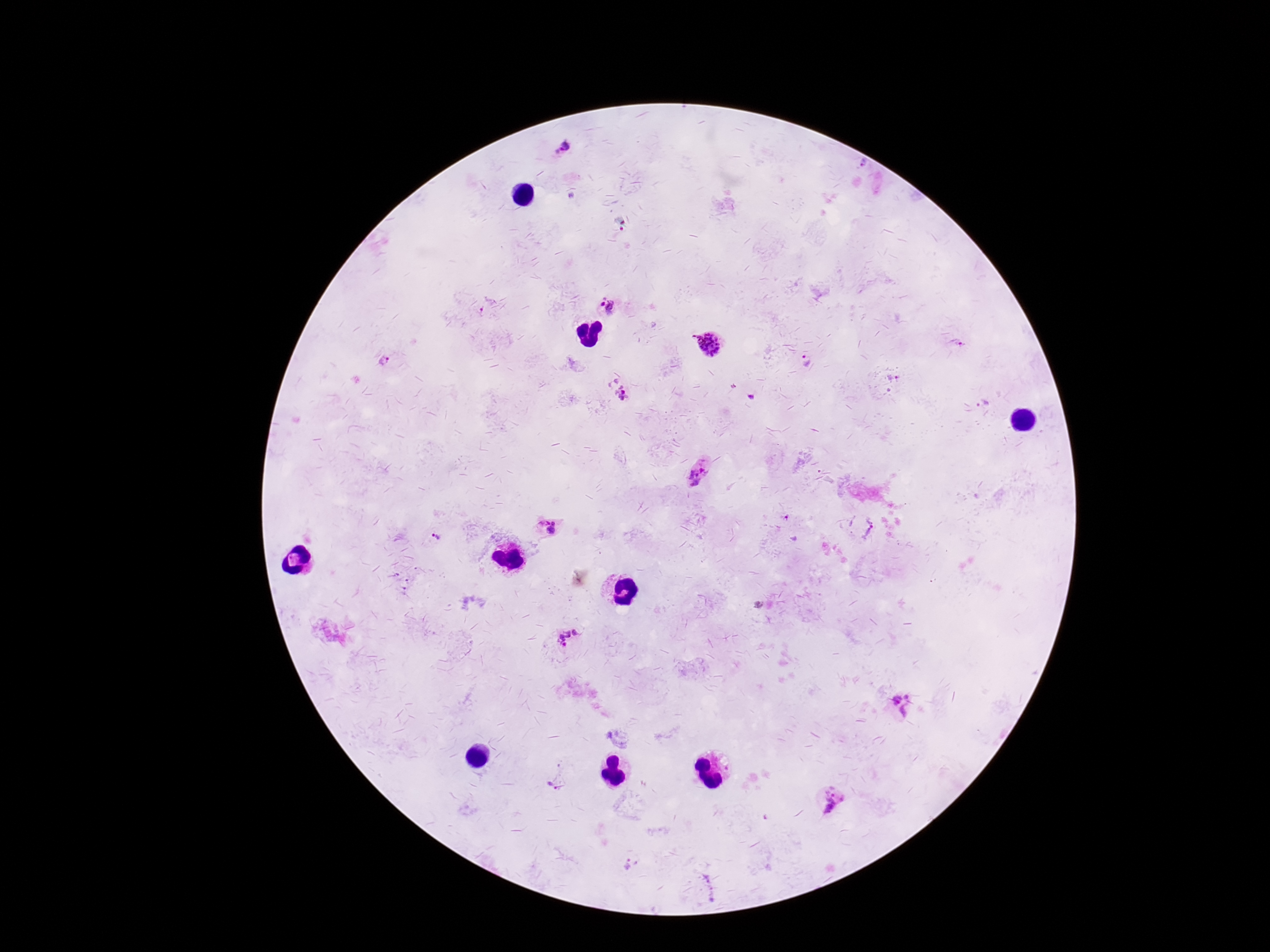
Approximate centers as [x, y] in pixels. Plasmodium parasite locations: [565, 144], [865, 164], [571, 196], [603, 304], [614, 308], [482, 310], [960, 343], [708, 344], [384, 360], [805, 362], [893, 378], [616, 388], [752, 397], [984, 401], [700, 475], [787, 519], [544, 522], [553, 522], [869, 529], [551, 531], [436, 537], [794, 539], [569, 639], [907, 696], [897, 700], [907, 711], [551, 786], [833, 800], [628, 864]. Single field of view. Patient malaria status: positive. Thick blood film. Photographed through the microscope eyepiece with a smartphone camera. Image is 1270×952 pixels. Giemsa stain. 100x magnification.